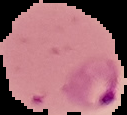

image size = 127×115 pixels
preparation = thin blood smear
result = Plasmodium parasites identified
image type = segmented cell region with the area outside set to black